Assess the morphology of the erythrocytes.
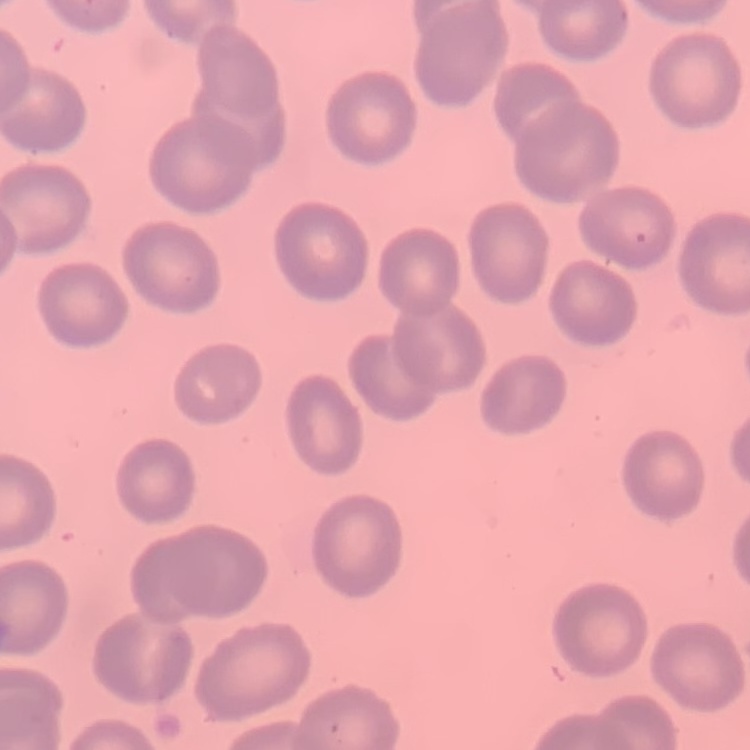

They show no rouleaux formation.

{
  "preparation": "thin blood smear",
  "image_type": "square crop of a larger photomicrograph",
  "stain": "Field's or Giemsa"
}